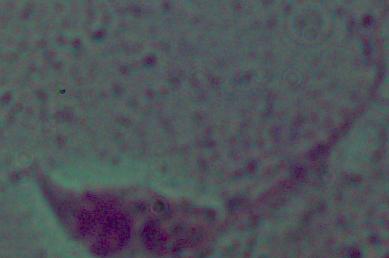
modality = micrograph
magnification = 1000x
identification = Leishmania